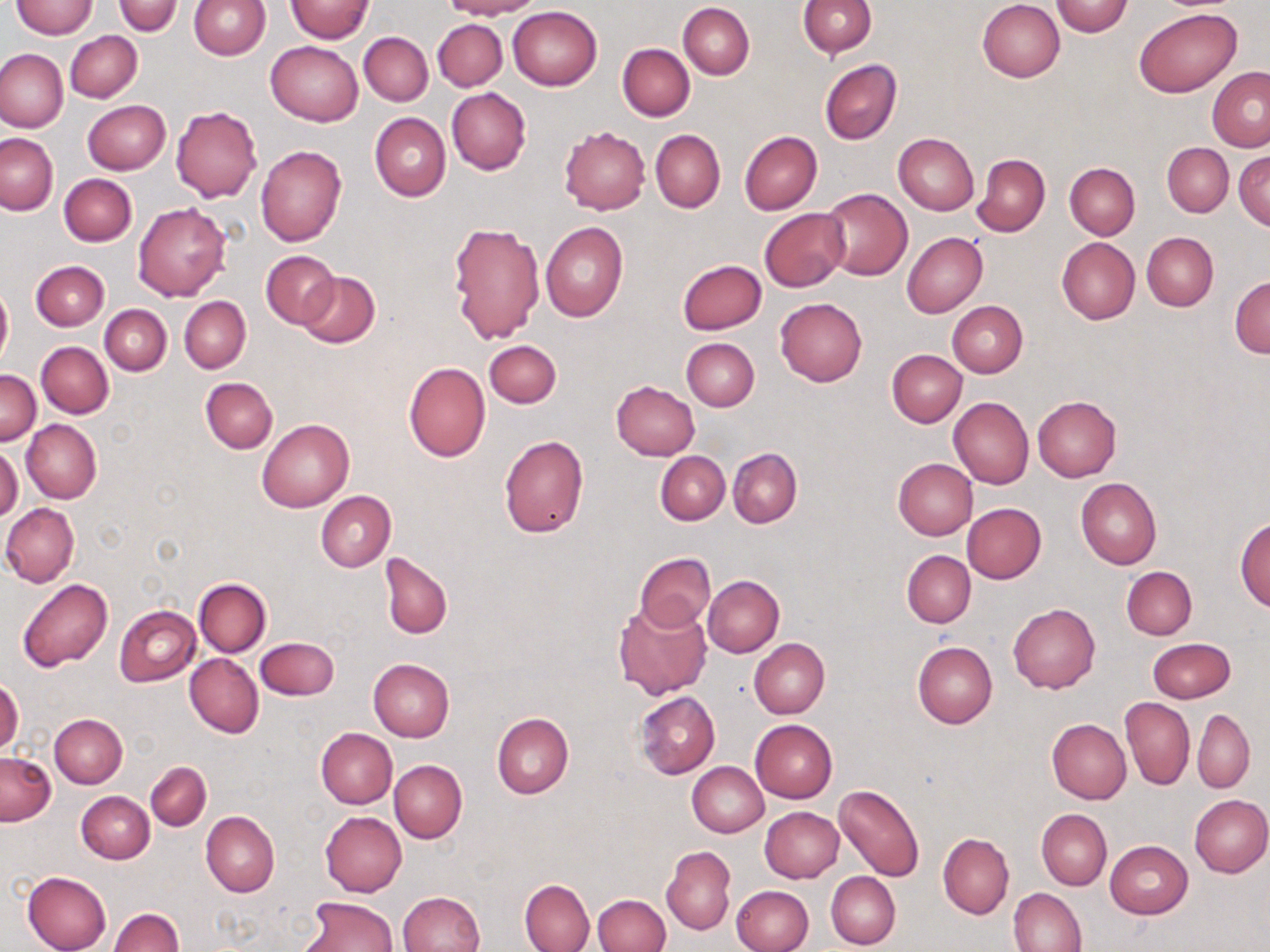 Approximate bounding boxes as (x1,y1)-(x2,y2) corner pairs in pixels. Uninfected red blood cell locations: (188,0)-(270,60), (286,0)-(374,43), (442,0)-(539,19), (798,0)-(876,57), (977,0)-(1065,82), (10,1)-(98,38), (111,1)-(183,36), (1051,1)-(1134,36), (678,3)-(754,79), (508,6)-(602,90), (1135,8)-(1239,98), (433,19)-(508,91), (65,31)-(142,102), (359,32)-(433,106), (265,41)-(363,126), (617,44)-(695,121), (0,49)-(67,132), (820,59)-(902,145), (1207,66)-(1270,151), (446,87)-(530,175), (83,101)-(170,175), (171,106)-(261,203), (67,109)-(144,245), (369,112)-(450,201), (560,126)-(650,214), (651,130)-(725,212), (740,131)-(823,215), (1,133)-(58,215), (893,133)-(979,215), (1162,143)-(1233,217), (256,144)-(348,246), (1234,150)-(1269,232), (972,152)-(1051,236), (1064,163)-(1140,239), (59,174)-(136,246), (820,188)-(912,281), (133,202)-(231,301), (760,208)-(848,291), (448,222)-(544,345), (541,223)-(628,322), (902,232)-(987,316), (1142,232)-(1218,311), (1058,238)-(1140,324), (261,251)-(339,329), (31,260)-(109,331), (678,260)-(766,335), (295,272)-(379,348), (1229,276)-(1270,359), (0,284)-(12,370), (180,296)-(250,373), (775,299)-(867,387), (948,301)-(1027,377), (100,304)-(171,375), (680,338)-(760,411), (484,339)-(561,408), (36,342)-(113,417), (886,349)-(966,427), (403,362)-(491,461), (0,371)-(41,444), (201,377)-(278,452), (611,380)-(699,460), (949,397)-(1033,489), (1031,397)-(1121,481), (257,419)-(353,513), (22,420)-(101,502), (498,434)-(589,538), (0,445)-(22,522), (728,448)-(802,528), (656,451)-(730,525), (893,458)-(977,540), (1076,478)-(1161,570), (315,491)-(395,571), (1,502)-(80,587), (963,503)-(1046,583), (1234,516)-(1270,611), (902,550)-(976,628), (634,552)-(716,632), (381,554)-(452,639), (1122,565)-(1197,639), (703,575)-(784,657), (18,577)-(112,672), (194,577)-(271,657), (613,601)-(712,700), (1007,603)-(1100,694), (115,605)-(201,687), (255,637)-(339,700), (750,638)-(830,718), (1148,638)-(1235,703), (912,642)-(997,729), (185,654)-(263,737), (368,659)-(455,740), (1,678)-(24,755), (635,691)-(720,778), (1120,697)-(1194,790), (1193,709)-(1255,792), (492,713)-(574,798), (50,714)-(127,788), (1047,718)-(1131,804), (751,719)-(838,802), (315,728)-(397,807), (1,752)-(56,825), (389,760)-(467,843), (146,761)-(211,830), (687,761)-(768,837), (834,783)-(925,882), (76,792)-(154,864), (1189,794)-(1270,877), (759,807)-(844,882), (1037,809)-(1112,889), (320,811)-(407,897), (201,812)-(280,897), (938,833)-(1014,919), (1105,840)-(1193,918), (662,848)-(735,933), (22,871)-(112,952), (826,871)-(901,949), (520,879)-(595,952), (731,885)-(813,952), (1008,887)-(1087,952), (398,891)-(484,952), (593,894)-(670,952), (300,896)-(396,952), (109,908)-(184,952). Slide-level diagnosis: negative for blood parasites. Thin blood smear. One field of a larger specimen. May-Grünwald-Giemsa-stained preparation. Light microscopy. Image is 1270×952 pixels. Captured at 1000x magnification.